State which parasite is depicted.
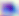

This is Toxoplasma gondii.

Summary:
  - Modality: photomicrograph
  - Magnification: 400x